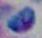

Summary:
  - Magnification: 1000x
  - Identification: Toxoplasma gondii
  - Modality: photomicrograph